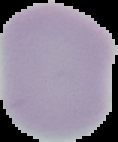

Summary:
  - Image type: cell region segmented out of the field of view; surrounding area masked to black
  - Preparation: thin blood film
  - Result: no malaria parasites seen
  - Image size: 118×142 pixels